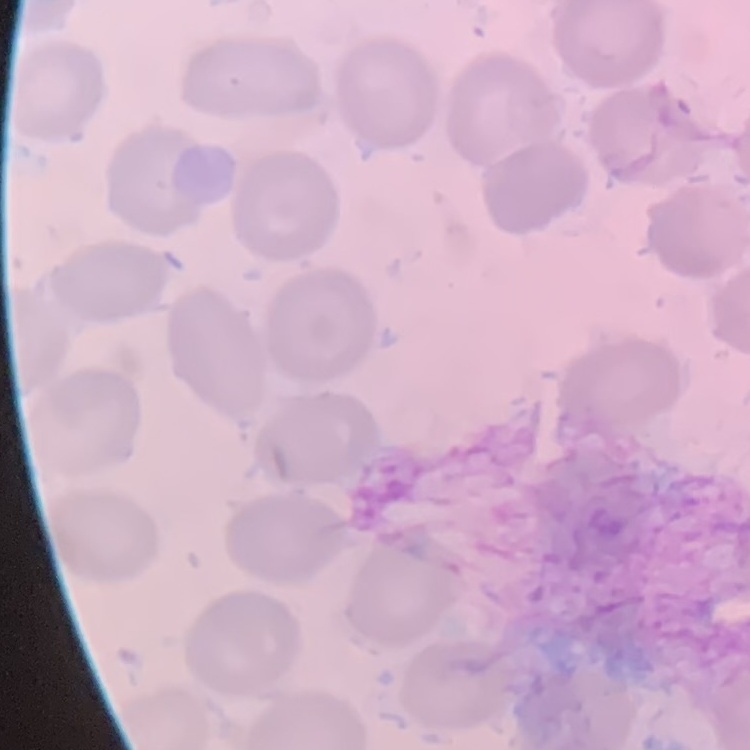
Summary:
  - Red blood cell morphology: no rouleaux formation
  - Preparation: thin peripheral smear
  - Image type: square crop of a larger photomicrograph
  - Stain: Field's or Giemsa